Classify this cell by malaria status.
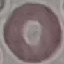

It is uninfected.

Summary:
  - Preparation: thin blood film
  - Capture: smartphone through the microscope eyepiece
  - Stain: Giemsa
  - Image type: automatically extracted cell patch, resized to 64 × 64 pixels